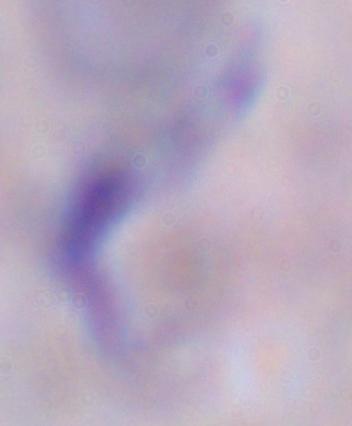
identification = trypanosome
modality = micrograph
magnification = 1000x